Assess the morphology of the red blood cells.
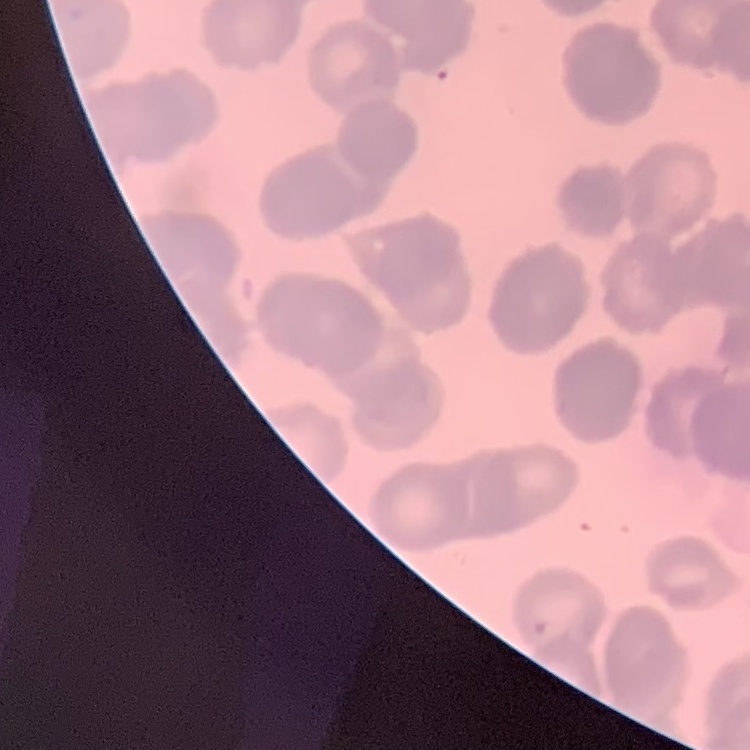

Rouleaux formation.

image type = square crop of a larger photomicrograph
preparation = thin blood film
stain = Field's or Giemsa